Name the blood parasite species.
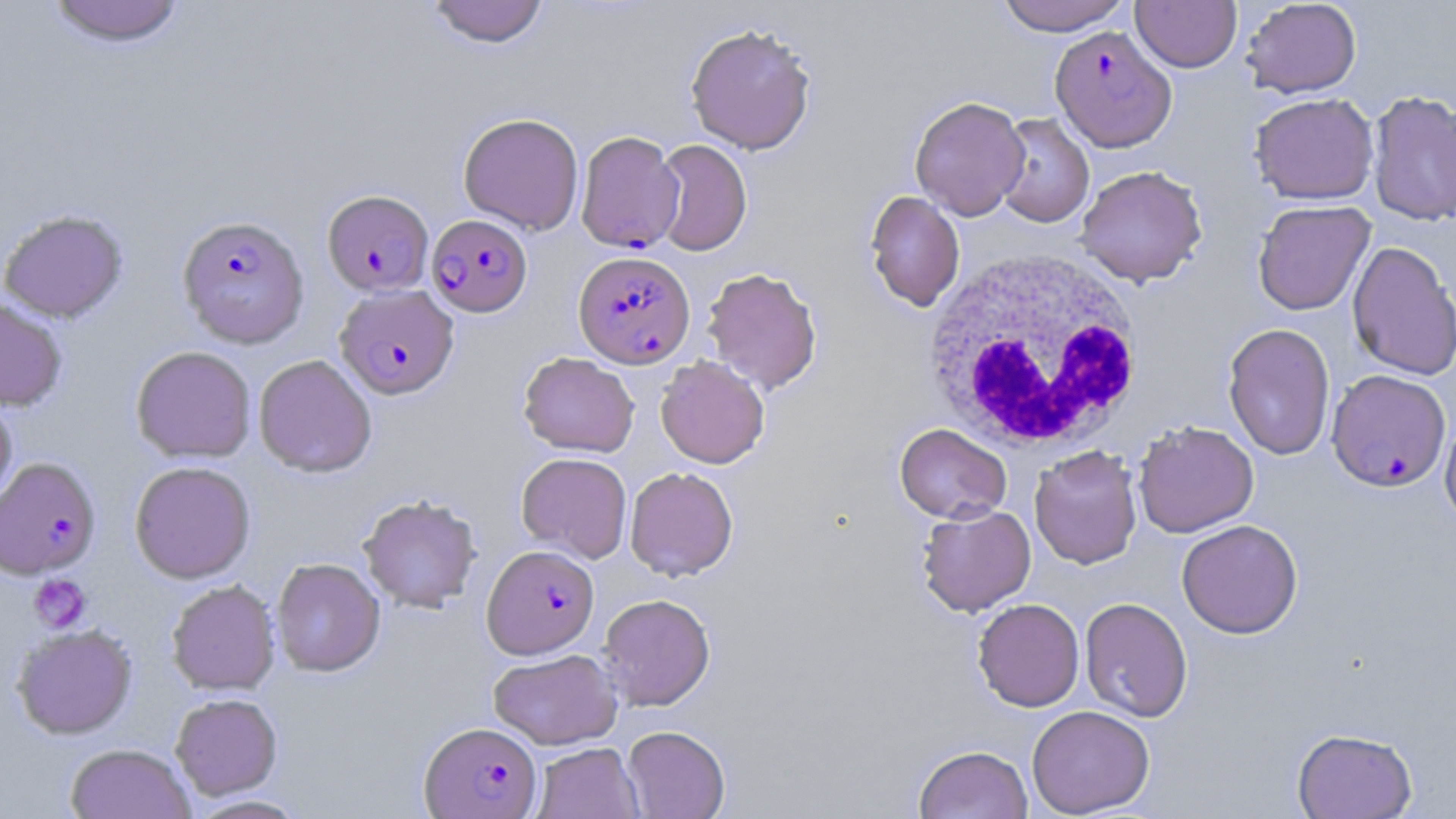
Plasmodium falciparum.

white_blood_cell_locations: 'approximate bounding boxes as (x1, y1, x2, y2) in pixels: (922, 248, 1145, 456)'
modality: optical microscopy
preparation: thin blood film
plasmodium_falciparum_infected_red_blood_cell_locations: 'approximate bounding boxes as (x1, y1, x2, y2) in pixels: (1049, 25, 1177, 152), (575, 130, 684, 253), (322, 190, 434, 296), (177, 215, 310, 348), (426, 215, 533, 317), (573, 250, 695, 368), (334, 285, 459, 400), (1326, 369, 1452, 493), (0, 457, 101, 581), (483, 545, 598, 658), (419, 722, 542, 818)'
platelet_locations: 'approximate bounding boxes as (x1, y1, x2, y2) in pixels: (28, 573, 90, 633)'
field_of_view: single
magnification: 1000x
image_size: 1456×819 pixels
stain: May-Grünwald-Giemsa
uninfected_red_blood_cell_locations: 'approximate bounding boxes as (x1, y1, x2, y2) in pixels: (427, 0, 549, 48), (994, 0, 1132, 36), (1131, 0, 1242, 73), (1240, 0, 1362, 98), (44, 1, 187, 50), (684, 22, 817, 155), (1366, 89, 1456, 227), (1249, 93, 1379, 205), (909, 95, 1030, 220), (458, 112, 584, 235), (992, 113, 1095, 228), (651, 139, 752, 256), (1075, 165, 1208, 287), (864, 190, 965, 311), (1252, 200, 1376, 315), (0, 209, 129, 323), (1347, 240, 1456, 380), (701, 266, 823, 394), (0, 298, 68, 411), (1222, 322, 1336, 461), (130, 346, 257, 463), (518, 352, 639, 457), (253, 354, 378, 478), (655, 355, 770, 469), (0, 393, 17, 514), (1440, 410, 1456, 532), (1133, 420, 1259, 538), (894, 423, 1012, 524), (1029, 445, 1142, 569), (516, 452, 632, 563), (129, 461, 256, 584), (625, 466, 739, 581), (358, 494, 482, 613), (917, 504, 1036, 616), (1176, 519, 1303, 639), (271, 558, 385, 677), (166, 580, 281, 696), (598, 593, 715, 711), (1080, 597, 1193, 722), (972, 598, 1085, 712), (11, 624, 138, 740), (488, 648, 622, 749), (170, 694, 283, 801), (1026, 705, 1155, 817), (622, 725, 730, 818), (1292, 728, 1418, 819), (532, 742, 644, 819), (65, 744, 196, 819), (913, 744, 1033, 819), (184, 795, 312, 818)'